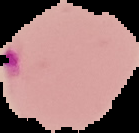

image type = segmented cell region with the area outside set to black
image size = 139×133 pixels
result = malaria parasites detected
preparation = thin blood smear